Give the position of each P. falciparum parasite with its life-cycle stage, each leukocyte, and any debris.
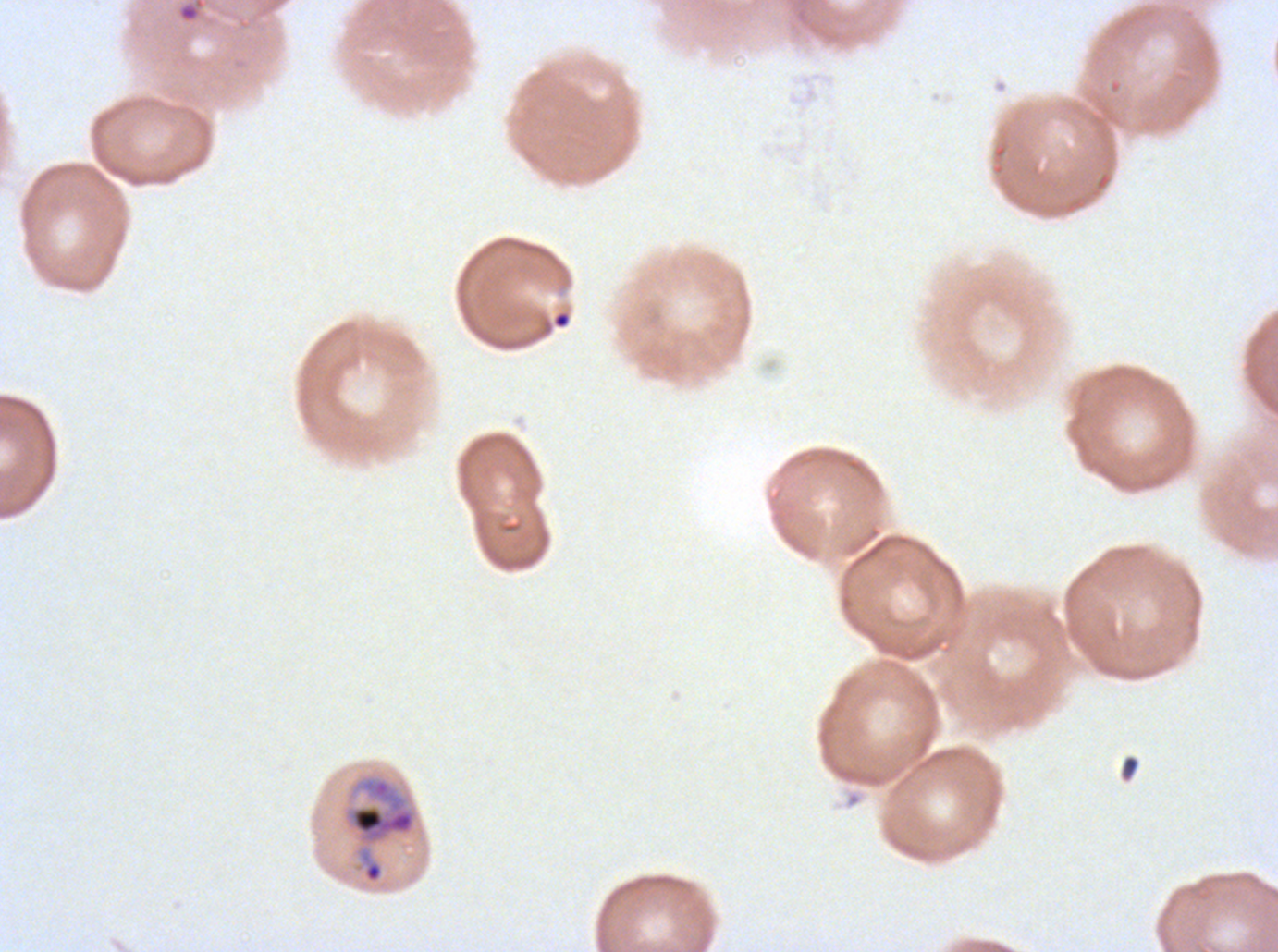

Approximate bounding boxes as [x1, y1, x2, y2] in pixels.
Mid trophozoites: [340, 771, 421, 885].
Debris: [178, 4, 199, 21], [552, 311, 571, 329], [1120, 754, 1139, 781].
No rings, late-ring/early-trophozoite forms, late trophozoites, early schizonts, late schizonts, segmenters, gametocytes, or leukocytes observed.

Summary:
  - Specimen: P. falciparum from a patient in The Gambia, cultured ex vivo for 24 to 48 hours
  - Field of view: sub-image separated from a larger composite
  - Preparation: thin blood film
  - Image size: 1278×952 pixels
  - Stain: Giemsa